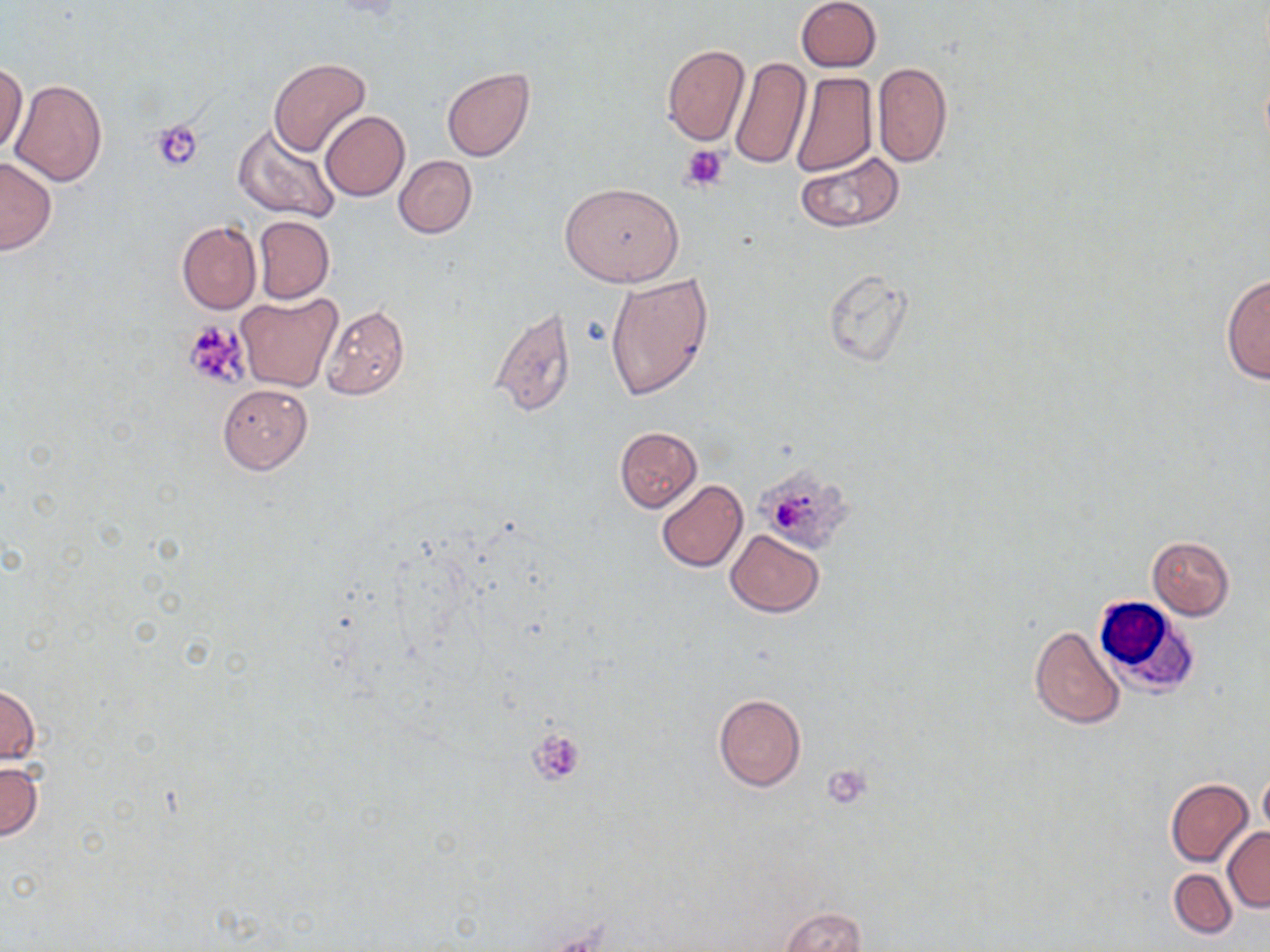

Approximate bounding boxes as named x1/y1/x2/y2 corners in pixels. Platelet locations: (x1=152, y1=120, x2=204, y2=171), (x1=681, y1=143, x2=731, y2=191), (x1=182, y1=320, x2=251, y2=388), (x1=759, y1=466, x2=852, y2=551), (x1=529, y1=729, x2=586, y2=785), (x1=822, y1=765, x2=873, y2=809). White blood cell locations: (x1=1093, y1=597, x2=1201, y2=699). Uninfected red blood cell locations: (x1=796, y1=0, x2=882, y2=71), (x1=660, y1=44, x2=751, y2=146), (x1=268, y1=57, x2=371, y2=158), (x1=731, y1=57, x2=810, y2=173), (x1=1, y1=60, x2=26, y2=156), (x1=872, y1=62, x2=953, y2=168), (x1=442, y1=69, x2=534, y2=162), (x1=789, y1=72, x2=877, y2=175), (x1=11, y1=79, x2=108, y2=186), (x1=320, y1=111, x2=410, y2=201), (x1=233, y1=123, x2=341, y2=224), (x1=795, y1=150, x2=906, y2=233), (x1=394, y1=155, x2=477, y2=238), (x1=0, y1=157, x2=57, y2=255), (x1=559, y1=180, x2=685, y2=286), (x1=253, y1=215, x2=335, y2=304), (x1=177, y1=220, x2=261, y2=314), (x1=823, y1=269, x2=913, y2=367), (x1=605, y1=272, x2=715, y2=401), (x1=1222, y1=272, x2=1269, y2=386), (x1=238, y1=293, x2=344, y2=393), (x1=320, y1=303, x2=409, y2=399), (x1=487, y1=306, x2=576, y2=417), (x1=217, y1=384, x2=312, y2=474), (x1=614, y1=427, x2=701, y2=512), (x1=656, y1=480, x2=748, y2=572), (x1=726, y1=530, x2=824, y2=616), (x1=1147, y1=536, x2=1236, y2=620), (x1=1029, y1=624, x2=1124, y2=730), (x1=1, y1=682, x2=41, y2=767), (x1=713, y1=693, x2=805, y2=791), (x1=0, y1=760, x2=43, y2=841), (x1=1258, y1=771, x2=1270, y2=837), (x1=1166, y1=778, x2=1253, y2=866), (x1=1222, y1=828, x2=1270, y2=911), (x1=1169, y1=869, x2=1235, y2=939), (x1=781, y1=907, x2=867, y2=952). Slide-level diagnosis: negative for blood parasites. Thin blood smear. One field of a larger specimen. 1000x magnification. Light microscopy. May-Grünwald-Giemsa stain. Image is 1270×952 pixels.